Locate every blood parasite and identify its species.
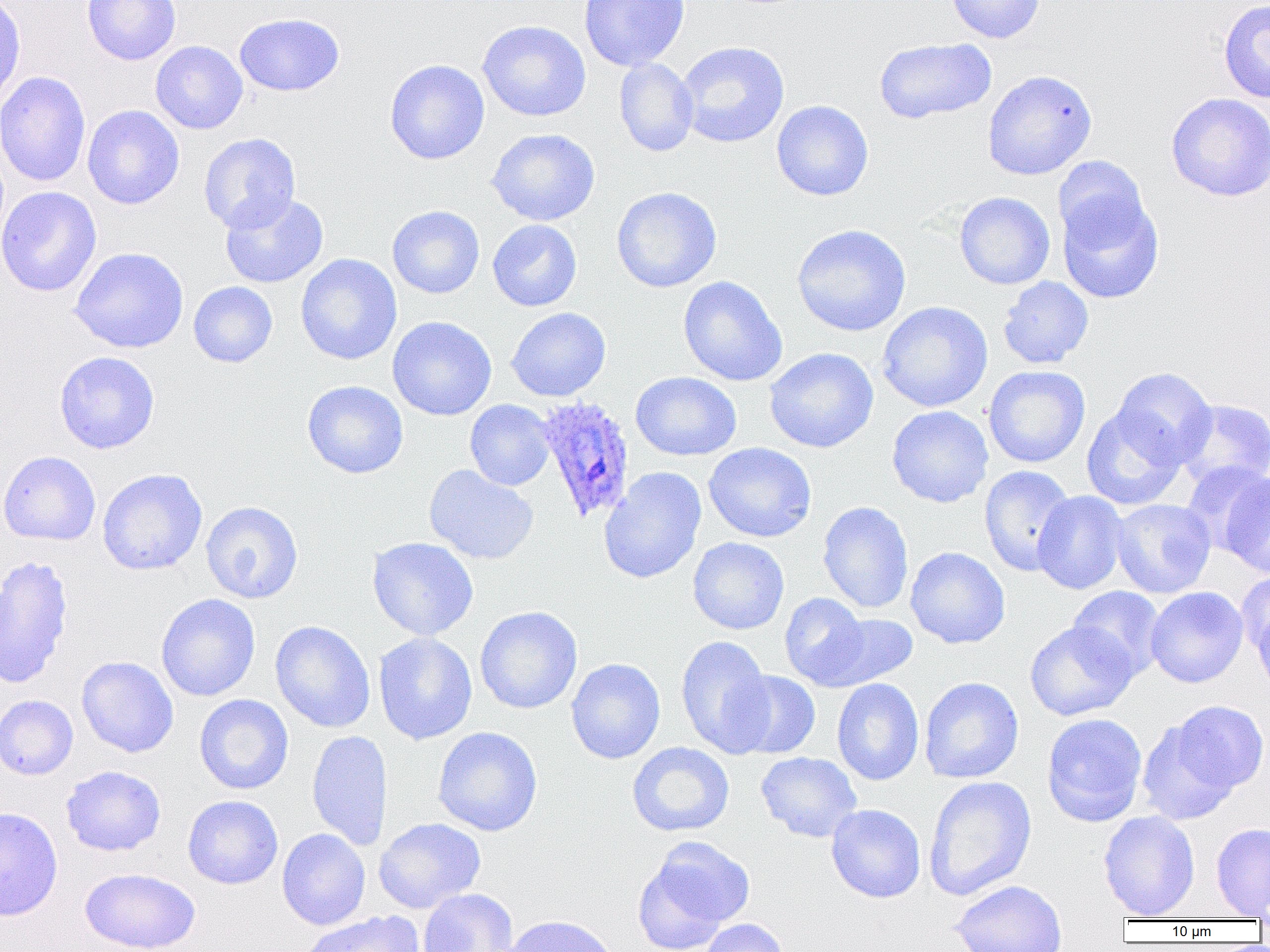

Approximate bounding boxes as named x1/y1/x2/y2 corners in pixels.
Plasmodium ovale-infected red blood cells: (x1=535, y1=397, x2=636, y2=525).
No Plasmodium falciparum, Plasmodium malariae, Plasmodium vivax, Babesia divergens, or Trypanosoma brucei observed.

Summary:
  - Uninfected red blood cell locations: (x1=0, y1=0, x2=26, y2=110), (x1=82, y1=0, x2=181, y2=65), (x1=579, y1=0, x2=689, y2=71), (x1=946, y1=0, x2=1046, y2=43), (x1=1218, y1=0, x2=1270, y2=103), (x1=234, y1=13, x2=345, y2=97), (x1=476, y1=20, x2=591, y2=122), (x1=874, y1=37, x2=996, y2=124), (x1=150, y1=41, x2=248, y2=134), (x1=676, y1=41, x2=789, y2=148), (x1=614, y1=57, x2=699, y2=157), (x1=384, y1=59, x2=490, y2=164), (x1=982, y1=69, x2=1097, y2=180), (x1=0, y1=71, x2=91, y2=187), (x1=1166, y1=92, x2=1270, y2=201), (x1=772, y1=100, x2=874, y2=201), (x1=82, y1=105, x2=185, y2=209), (x1=486, y1=128, x2=600, y2=226), (x1=198, y1=133, x2=301, y2=233), (x1=1053, y1=156, x2=1150, y2=249), (x1=0, y1=186, x2=102, y2=296), (x1=611, y1=186, x2=722, y2=293), (x1=219, y1=192, x2=329, y2=289), (x1=954, y1=192, x2=1055, y2=290), (x1=1057, y1=192, x2=1164, y2=304), (x1=387, y1=205, x2=485, y2=299), (x1=487, y1=219, x2=582, y2=311), (x1=791, y1=224, x2=912, y2=336), (x1=69, y1=247, x2=189, y2=354), (x1=296, y1=254, x2=402, y2=365), (x1=678, y1=276, x2=788, y2=386), (x1=998, y1=276, x2=1094, y2=369), (x1=188, y1=281, x2=277, y2=367), (x1=876, y1=301, x2=993, y2=412), (x1=506, y1=307, x2=611, y2=402), (x1=387, y1=316, x2=496, y2=421), (x1=764, y1=347, x2=879, y2=453), (x1=54, y1=351, x2=159, y2=454), (x1=983, y1=366, x2=1090, y2=468), (x1=1112, y1=367, x2=1217, y2=467), (x1=630, y1=371, x2=741, y2=461), (x1=302, y1=380, x2=408, y2=478), (x1=464, y1=399, x2=555, y2=490), (x1=1176, y1=399, x2=1270, y2=491), (x1=886, y1=405, x2=993, y2=508), (x1=1082, y1=405, x2=1186, y2=510), (x1=703, y1=443, x2=817, y2=542), (x1=0, y1=450, x2=101, y2=546), (x1=1180, y1=461, x2=1270, y2=557), (x1=423, y1=464, x2=539, y2=565), (x1=979, y1=465, x2=1077, y2=576), (x1=599, y1=467, x2=706, y2=584), (x1=97, y1=468, x2=208, y2=576), (x1=1222, y1=472, x2=1270, y2=579), (x1=1032, y1=490, x2=1128, y2=594), (x1=1111, y1=498, x2=1216, y2=598), (x1=201, y1=501, x2=304, y2=604), (x1=817, y1=501, x2=914, y2=614), (x1=367, y1=536, x2=479, y2=641), (x1=688, y1=537, x2=789, y2=634), (x1=905, y1=546, x2=1010, y2=649), (x1=0, y1=555, x2=74, y2=689), (x1=1235, y1=572, x2=1270, y2=659), (x1=1067, y1=586, x2=1165, y2=680), (x1=1145, y1=586, x2=1248, y2=688), (x1=779, y1=592, x2=871, y2=688), (x1=156, y1=594, x2=260, y2=702), (x1=1253, y1=602, x2=1270, y2=699), (x1=474, y1=606, x2=583, y2=714), (x1=817, y1=613, x2=918, y2=690), (x1=270, y1=620, x2=375, y2=733), (x1=1025, y1=621, x2=1139, y2=721), (x1=373, y1=632, x2=477, y2=745), (x1=675, y1=635, x2=775, y2=757), (x1=76, y1=656, x2=179, y2=758), (x1=566, y1=658, x2=666, y2=764), (x1=728, y1=670, x2=821, y2=759), (x1=919, y1=677, x2=1023, y2=784), (x1=832, y1=678, x2=924, y2=785), (x1=194, y1=694, x2=293, y2=795), (x1=0, y1=695, x2=78, y2=780), (x1=1169, y1=700, x2=1268, y2=794), (x1=1042, y1=712, x2=1147, y2=827), (x1=1137, y1=718, x2=1240, y2=825), (x1=432, y1=726, x2=543, y2=836), (x1=306, y1=730, x2=392, y2=850), (x1=627, y1=742, x2=734, y2=837), (x1=755, y1=752, x2=862, y2=843), (x1=61, y1=765, x2=166, y2=856), (x1=924, y1=775, x2=1037, y2=901), (x1=182, y1=795, x2=283, y2=889), (x1=826, y1=804, x2=926, y2=903), (x1=0, y1=806, x2=63, y2=921), (x1=1099, y1=811, x2=1200, y2=919), (x1=374, y1=818, x2=486, y2=913), (x1=1211, y1=822, x2=1270, y2=918), (x1=277, y1=828, x2=371, y2=930), (x1=638, y1=837, x2=754, y2=945), (x1=80, y1=867, x2=201, y2=952), (x1=950, y1=879, x2=1067, y2=952), (x1=418, y1=888, x2=519, y2=952), (x1=300, y1=911, x2=424, y2=952), (x1=501, y1=914, x2=619, y2=952), (x1=698, y1=918, x2=790, y2=952)
  - Slide-level diagnosis: Plasmodium ovale
  - Modality: light microscopy
  - Preparation: thin blood smear
  - Image size: 1270×952 pixels
  - Magnification: 1000x
  - Field of view: single